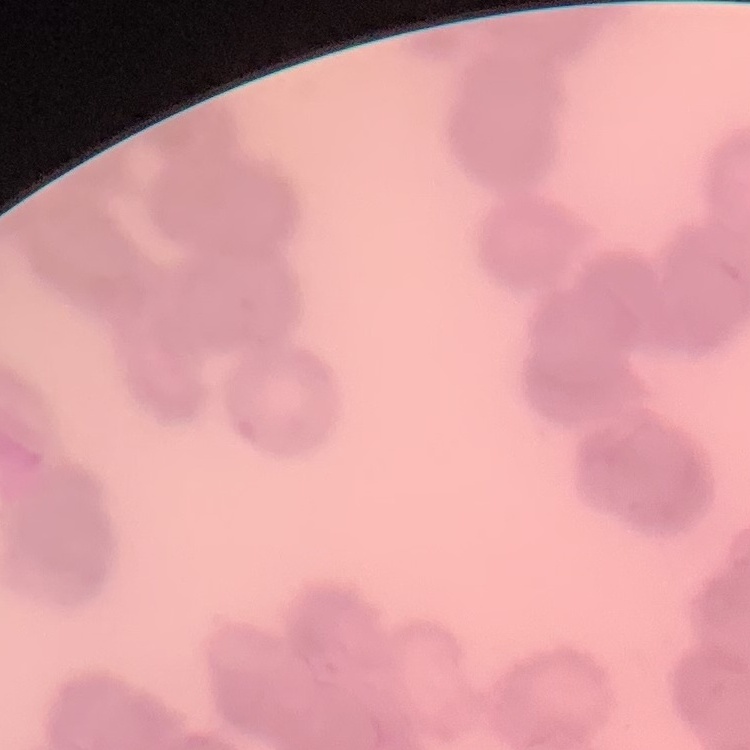

The erythrocytes exhibit rouleaux formation. Thin blood smear. Stained with either Field's or Giemsa. Square crop of a larger photomicrograph.